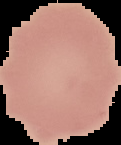
image type = segmented cell region with the area outside set to black
image size = 121×145 pixels
preparation = thin blood film
malaria status = uninfected